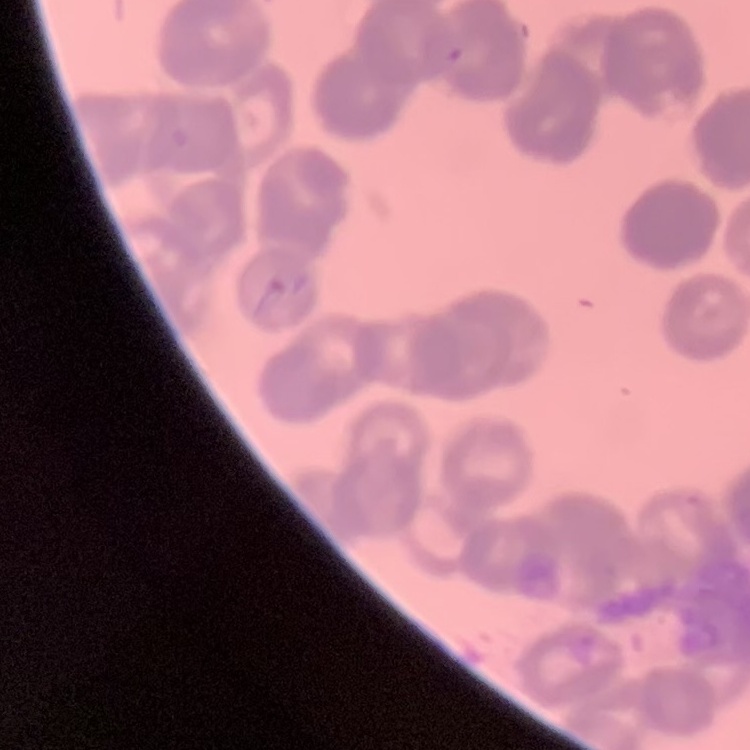

erythrocyte morphology = rouleaux formation
preparation = thin blood smear
stain = Field's or Giemsa
image type = one tile cut from a larger photomicrograph